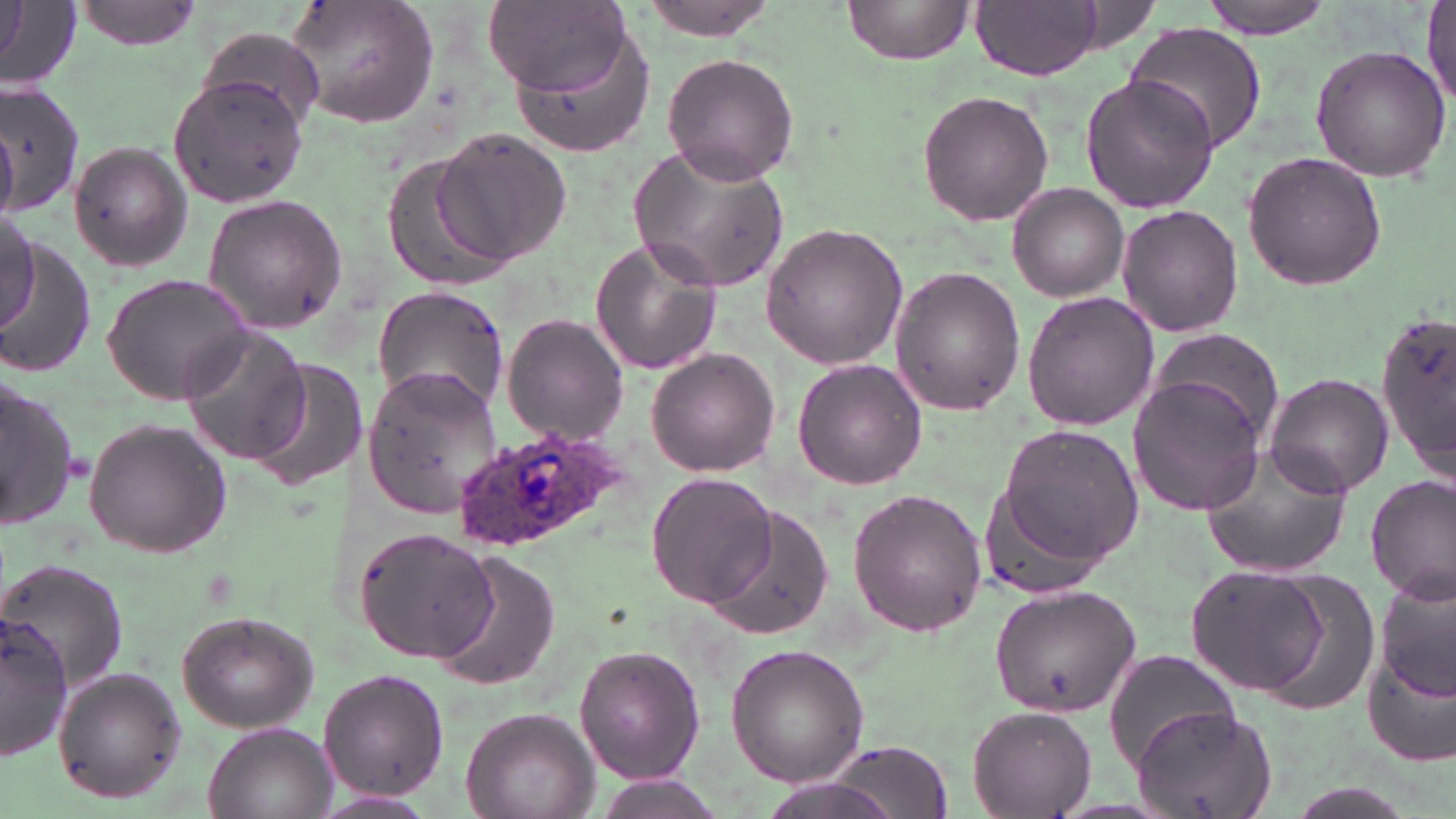

slide-level diagnosis = Plasmodium ovale
image size = 1456×819 pixels
Plasmodium ovale-infected red blood cell locations = approximate bounding boxes as (x1,y1)-(x2,y2) corner pairs in pixels: (450,426)-(635,553)
uninfected red blood cell locations = approximate bounding boxes as (x1,y1)-(x2,y2) corner pairs in pixels: (72,0)-(203,51), (284,0)-(443,130), (841,0)-(976,64), (971,0)-(1104,79), (1197,0)-(1335,38), (640,1)-(782,40), (487,2)-(633,99), (0,3)-(80,91), (1420,4)-(1455,109), (495,15)-(651,165), (1123,22)-(1269,156), (201,26)-(325,128), (1308,46)-(1450,182), (658,51)-(801,186), (168,71)-(308,212), (1082,73)-(1220,214), (0,82)-(84,218), (917,89)-(1054,225), (431,128)-(573,265), (70,140)-(192,272), (630,144)-(789,291), (1241,149)-(1391,293), (385,158)-(522,291), (1008,182)-(1127,301), (202,193)-(348,332), (1115,204)-(1243,337), (1,214)-(40,332), (759,222)-(909,370), (1,238)-(97,380), (588,238)-(724,375), (888,267)-(1025,416), (99,271)-(254,405), (372,285)-(512,412), (1021,290)-(1160,432), (1376,309)-(1456,484), (500,314)-(629,446), (1148,325)-(1284,446), (178,326)-(315,467), (647,348)-(779,475), (244,353)-(362,493), (793,358)-(927,490), (359,366)-(503,518), (0,373)-(83,528), (1262,373)-(1391,499), (1126,378)-(1262,517), (83,418)-(231,557), (993,422)-(1146,581), (1200,443)-(1353,578), (647,472)-(777,610), (1366,474)-(1455,606), (848,487)-(988,637), (982,488)-(1113,603), (708,504)-(837,640), (354,527)-(496,663), (432,551)-(560,691), (0,562)-(131,693), (1184,564)-(1332,695), (1250,568)-(1383,719), (1375,576)-(1455,706), (989,583)-(1140,718), (176,610)-(319,732), (2,614)-(73,761), (725,642)-(870,785), (575,644)-(705,786), (1363,647)-(1456,769), (1104,651)-(1243,772), (53,668)-(187,804), (318,669)-(448,801), (1132,703)-(1280,819), (971,705)-(1096,816), (460,707)-(600,819), (202,724)-(335,819), (826,740)-(957,818), (595,778)-(731,818)
preparation = thin blood smear
magnification = 1000x
stain = May-Grünwald-Giemsa
field of view = single
modality = optical microscopy